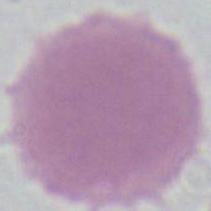

Photomicrograph. An erythrocyte is seen. 1000x magnification.